Classify this cell by malaria status.
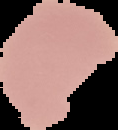
It is uninfected.

Summary:
  - Image type: segmented cell region on a black background
  - Image size: 118×130 pixels
  - Preparation: thin blood film